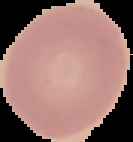

Malaria status: uninfected. Segmented cell region on a black background. Image is 133×142 pixels. From a thin blood film.